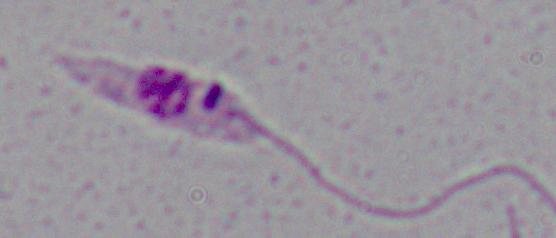

Micrograph. A Leishmania parasite is shown. 1000x magnification.